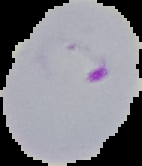
Summary:
  - Image type: cell region segmented out of the field of view; surrounding area masked to black
  - Malaria status: parasitized
  - Preparation: thin blood film
  - Image size: 142×166 pixels